Point out each malaria parasite.
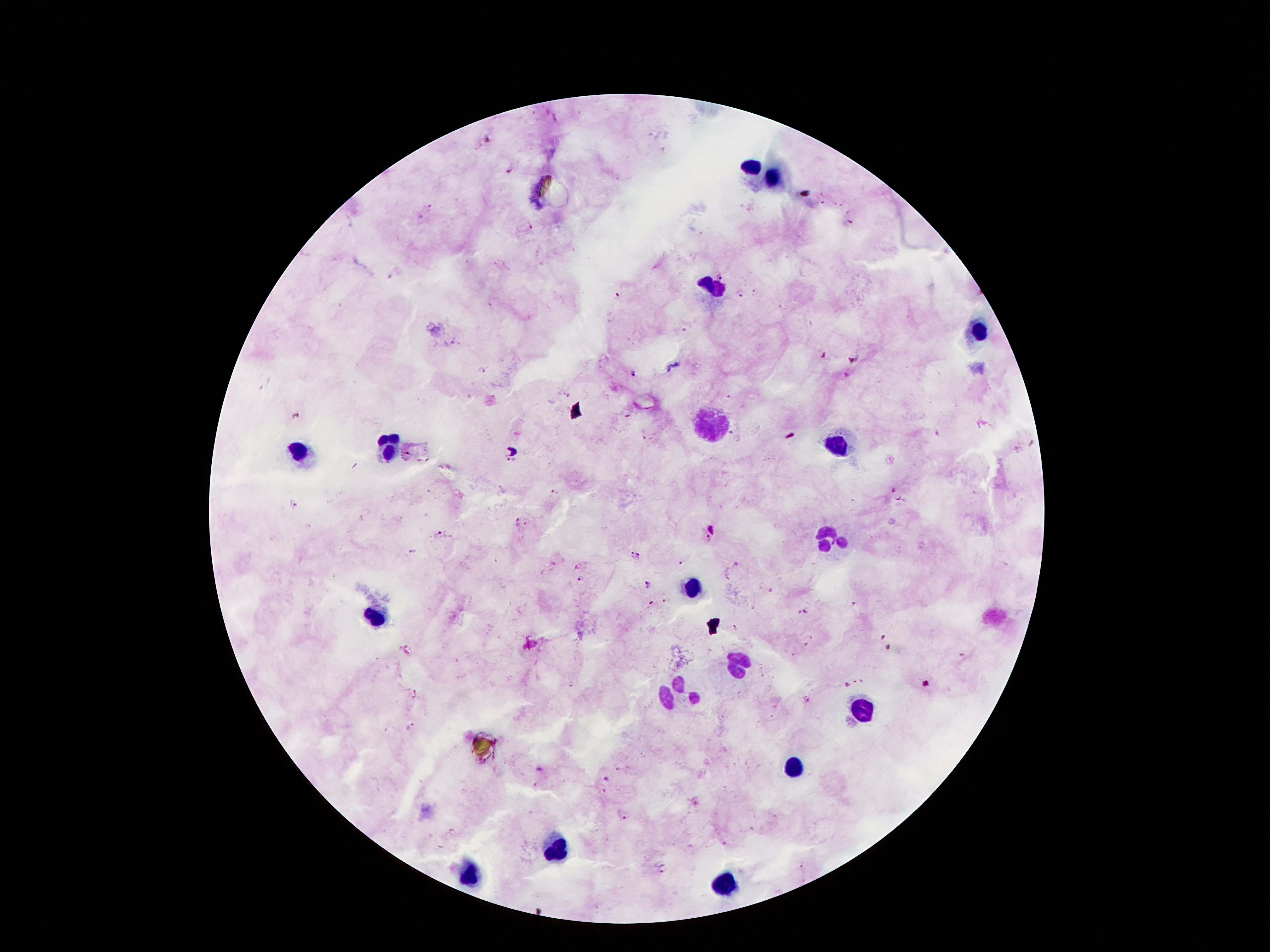

Approximate centers as [x, y] in pixels.
Malaria parasites: [720, 278], [741, 291], [616, 296], [483, 370], [634, 372], [294, 418], [512, 461], [893, 489], [898, 498], [294, 503], [517, 523], [527, 524], [710, 533], [441, 534], [411, 552], [635, 555], [681, 562], [577, 566], [582, 579], [649, 585], [664, 601], [651, 603], [623, 815].

Summary:
  - Leukocyte locations: [752, 167], [773, 180], [711, 287], [984, 334], [705, 424], [388, 444], [838, 445], [302, 453], [832, 537], [692, 585], [377, 617], [734, 661], [678, 691], [864, 707], [795, 766], [556, 849], [470, 875], [724, 884]
  - Field of view: one from this slide
  - Stain: Giemsa
  - Patient malaria status: infected with Plasmodium falciparum
  - Magnification: 100x
  - Preparation: thick blood film
  - Capture: smartphone through the microscope eyepiece
  - Image size: 1270×952 pixels